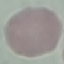

Result: no malaria parasites detected. Photographed with a smartphone camera at the microscope eyepiece. Cell patch, automatically extracted from a larger field of view and resized to 64 × 64 pixels. Giemsa-stained preparation. Thin blood film.